Identify the blood parasite species.
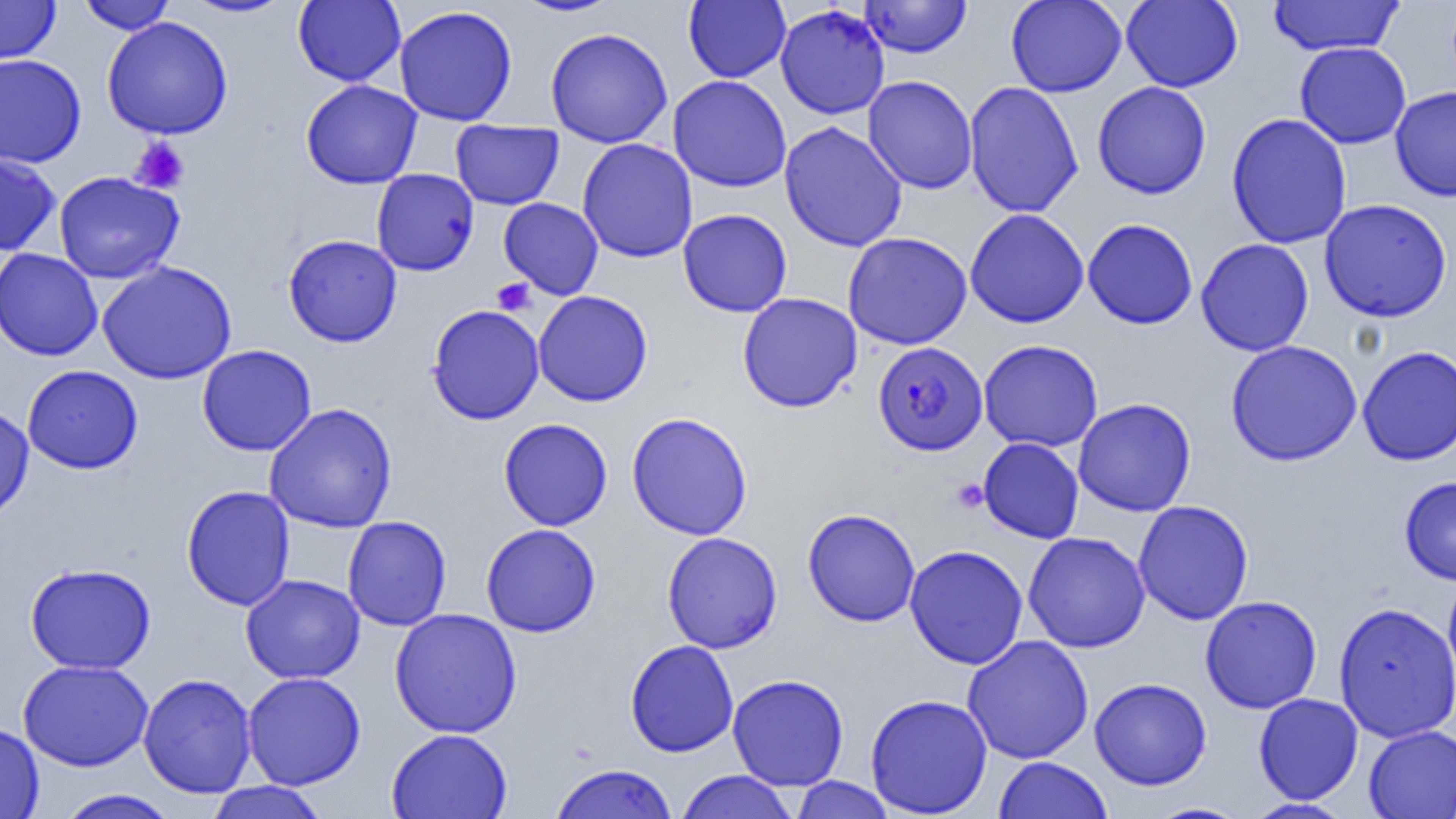

Plasmodium falciparum.

Summary:
  - Coordinate format: approximate bounding boxes as named x1/y1/x2/y2 corners in pixels
  - Plasmodium falciparum-infected red blood cell locations: (x1=873, y1=341, x2=987, y2=456)
  - Platelet locations: (x1=130, y1=138, x2=190, y2=194), (x1=491, y1=278, x2=537, y2=316), (x1=951, y1=478, x2=989, y2=514)
  - Uninfected red blood cell locations: (x1=0, y1=0, x2=61, y2=64), (x1=77, y1=0, x2=176, y2=34), (x1=182, y1=0, x2=295, y2=18), (x1=293, y1=0, x2=406, y2=87), (x1=512, y1=0, x2=624, y2=17), (x1=683, y1=0, x2=791, y2=83), (x1=860, y1=0, x2=971, y2=58), (x1=1005, y1=0, x2=1127, y2=97), (x1=1121, y1=0, x2=1243, y2=92), (x1=1267, y1=0, x2=1404, y2=56), (x1=394, y1=5, x2=518, y2=126), (x1=775, y1=5, x2=890, y2=119), (x1=102, y1=16, x2=233, y2=140), (x1=545, y1=27, x2=673, y2=148), (x1=1295, y1=42, x2=1411, y2=149), (x1=0, y1=54, x2=86, y2=168), (x1=668, y1=75, x2=792, y2=192), (x1=862, y1=75, x2=978, y2=194), (x1=301, y1=80, x2=422, y2=189), (x1=964, y1=81, x2=1084, y2=218), (x1=1092, y1=81, x2=1211, y2=199), (x1=1390, y1=85, x2=1456, y2=202), (x1=1226, y1=112, x2=1352, y2=249), (x1=450, y1=120, x2=564, y2=210), (x1=779, y1=121, x2=907, y2=252), (x1=577, y1=138, x2=698, y2=263), (x1=0, y1=150, x2=61, y2=256), (x1=371, y1=168, x2=479, y2=276), (x1=53, y1=171, x2=184, y2=283), (x1=498, y1=197, x2=604, y2=300), (x1=1319, y1=198, x2=1452, y2=322), (x1=677, y1=208, x2=792, y2=317), (x1=964, y1=208, x2=1090, y2=328), (x1=1082, y1=218, x2=1198, y2=330), (x1=842, y1=232, x2=973, y2=350), (x1=283, y1=233, x2=403, y2=347), (x1=1195, y1=238, x2=1314, y2=356), (x1=0, y1=248, x2=103, y2=361), (x1=97, y1=261, x2=237, y2=384), (x1=533, y1=290, x2=653, y2=407), (x1=737, y1=293, x2=862, y2=413), (x1=427, y1=304, x2=545, y2=425), (x1=978, y1=339, x2=1104, y2=452), (x1=1225, y1=339, x2=1363, y2=466), (x1=197, y1=344, x2=317, y2=456), (x1=1358, y1=345, x2=1456, y2=465), (x1=21, y1=365, x2=143, y2=474), (x1=1073, y1=398, x2=1197, y2=516), (x1=263, y1=402, x2=398, y2=533), (x1=0, y1=404, x2=34, y2=522), (x1=627, y1=412, x2=753, y2=540), (x1=498, y1=418, x2=613, y2=531), (x1=978, y1=437, x2=1084, y2=544), (x1=1399, y1=475, x2=1456, y2=585), (x1=181, y1=485, x2=295, y2=611), (x1=1132, y1=500, x2=1254, y2=625), (x1=803, y1=508, x2=921, y2=627), (x1=342, y1=516, x2=452, y2=631), (x1=481, y1=523, x2=601, y2=638), (x1=661, y1=531, x2=783, y2=654), (x1=1023, y1=531, x2=1150, y2=653), (x1=904, y1=545, x2=1029, y2=670), (x1=24, y1=563, x2=156, y2=674), (x1=1443, y1=570, x2=1456, y2=694), (x1=241, y1=574, x2=365, y2=684), (x1=1200, y1=595, x2=1322, y2=714), (x1=1333, y1=601, x2=1456, y2=744), (x1=389, y1=607, x2=523, y2=739), (x1=962, y1=635, x2=1094, y2=764), (x1=625, y1=639, x2=739, y2=757), (x1=18, y1=659, x2=154, y2=771), (x1=241, y1=672, x2=366, y2=789), (x1=138, y1=673, x2=257, y2=798), (x1=728, y1=673, x2=849, y2=791), (x1=1089, y1=677, x2=1211, y2=790), (x1=1253, y1=692, x2=1363, y2=804), (x1=864, y1=693, x2=993, y2=818), (x1=0, y1=723, x2=44, y2=819), (x1=1363, y1=725, x2=1456, y2=818), (x1=386, y1=728, x2=512, y2=819), (x1=993, y1=756, x2=1113, y2=819), (x1=548, y1=763, x2=679, y2=819), (x1=675, y1=770, x2=797, y2=819), (x1=788, y1=776, x2=897, y2=819), (x1=203, y1=781, x2=331, y2=819), (x1=55, y1=789, x2=180, y2=819), (x1=1244, y1=798, x2=1353, y2=819), (x1=1144, y1=802, x2=1253, y2=819)
  - Magnification: 1000x
  - Preparation: thin blood film
  - Field of view: single
  - Image size: 1456×819 pixels
  - Modality: optical microscopy